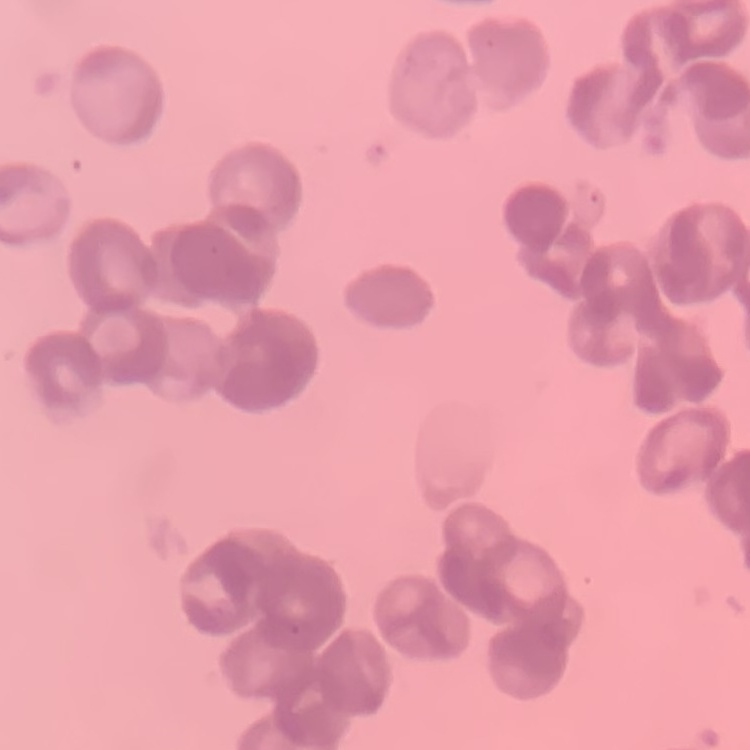

Summary:
  - Red blood cell morphology: rouleaux formation
  - Preparation: thin peripheral smear
  - Image type: square crop of a larger photomicrograph
  - Stain: Field's or Giemsa